Report the malaria status of this cell.
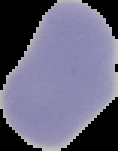
Uninfected.

Image is 118×151 pixels. The area outside the segmented cell region is set to black. From a thin blood smear.